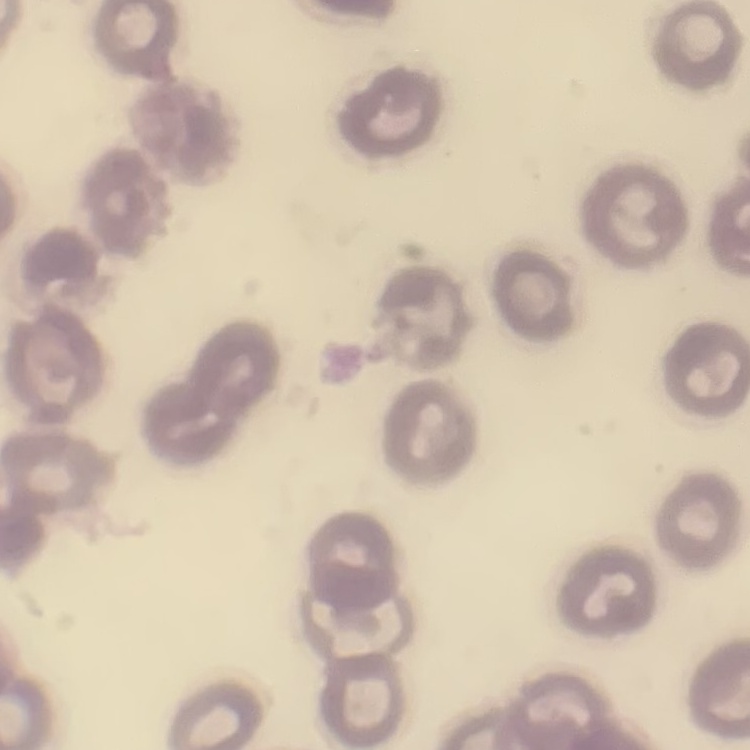

red blood cell morphology = no rouleaux formation
image type = square crop of a larger photomicrograph
stain = Field's or Giemsa
preparation = thin peripheral smear